Classify this cell by malaria status.
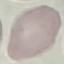

Uninfected.

Cell patch, automatically extracted from a larger field of view and resized to 64 × 64 pixels. Thin smear of blood. Giemsa stain. Photographed with a smartphone camera at the microscope eyepiece.